Assess this cell for malaria.
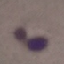

It is uninfected.

{
  "image_type": "automatically extracted cell patch, resized to 64 × 64 pixels",
  "preparation": "thin smear",
  "stain": "Giemsa",
  "capture": "smartphone camera at the microscope eyepiece"
}